Describe the morphology of the red blood cells.
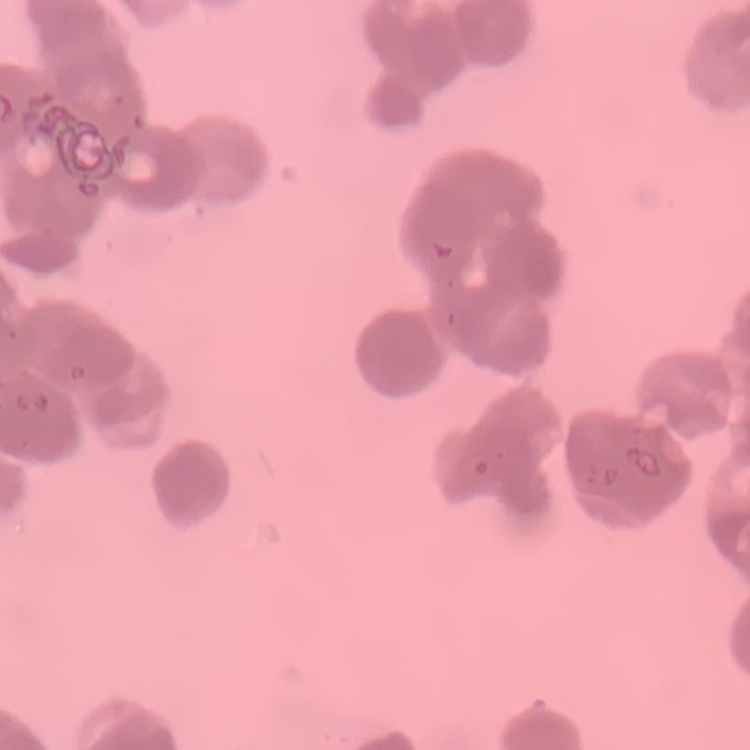

They show rouleaux formation.

{
  "preparation": "thin blood smear",
  "image_type": "one tile cut from a larger photomicrograph",
  "stain": "Field's or Giemsa"
}